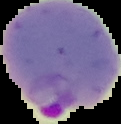
Summary:
  - Preparation: thin blood smear
  - Malaria status: parasitized
  - Image size: 121×124 pixels
  - Image type: segmented cell region on a black background